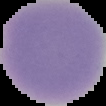

Malaria status: uninfected. The area outside the segmented cell region is set to black. Image is 106×106 pixels. From a thin blood film.